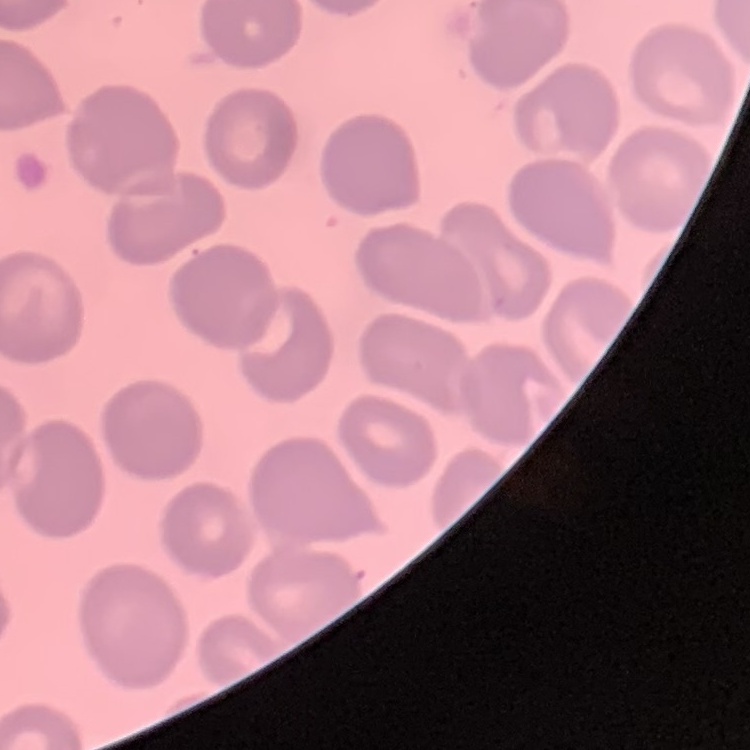
{
  "erythrocyte_morphology": "no rouleaux formation",
  "preparation": "thin peripheral smear",
  "image_type": "square crop of a larger photomicrograph",
  "stain": "Field's or Giemsa"
}